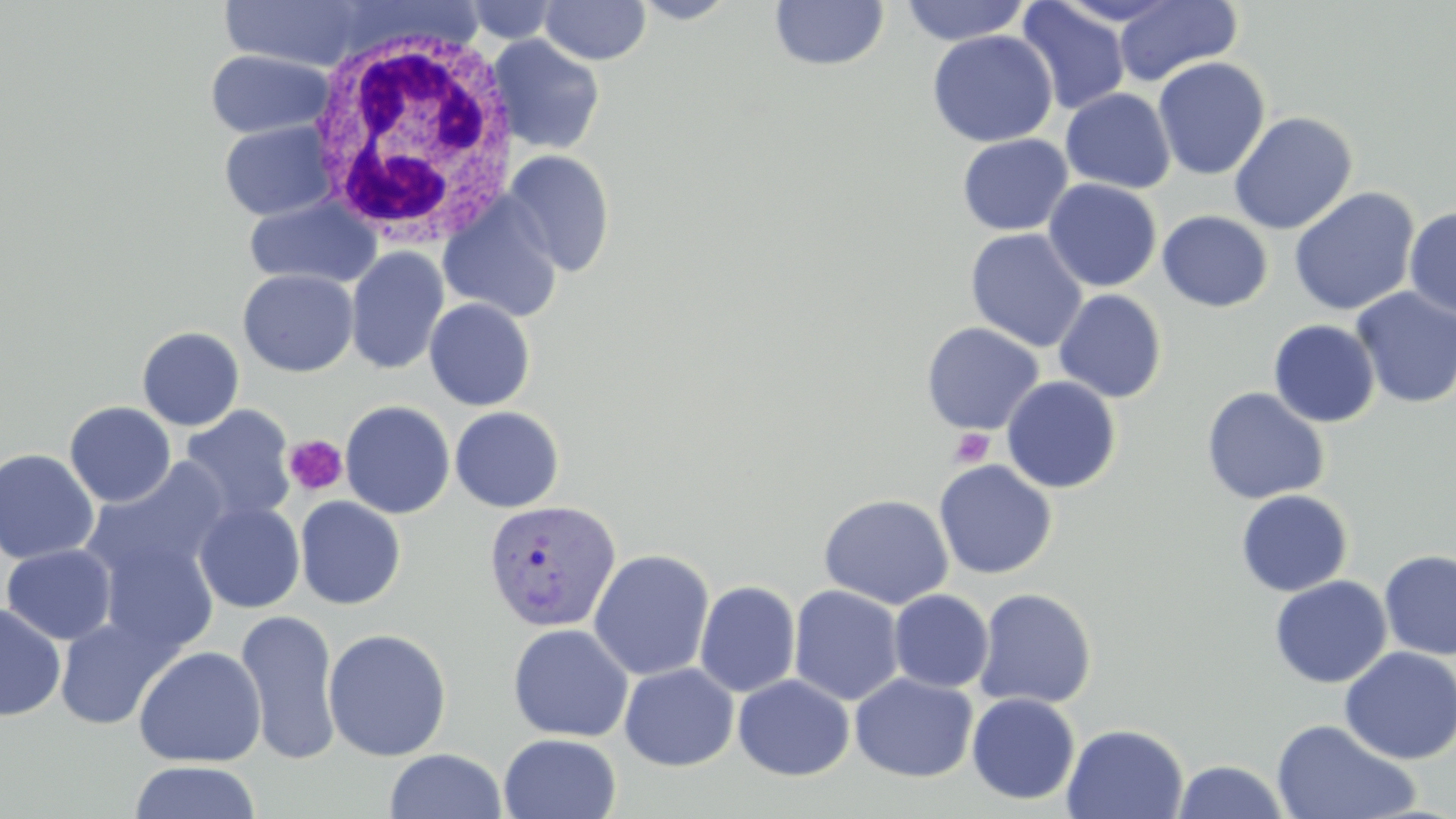

slide-level diagnosis = Plasmodium vivax
field of view = single
image size = 1456×819 pixels
white blood cell locations = approximate bounding boxes as [x1, y1, x2, y2] in pixels: [301, 24, 521, 251]
magnification = 1000x
preparation = thin blood smear
Plasmodium vivax-infected red blood cell locations = approximate bounding boxes as [x1, y1, x2, y2] in pixels: [482, 499, 622, 633]
uninfected red blood cell locations = approximate bounding boxes as [x1, y1, x2, y2] in pixels: [539, 0, 651, 65], [630, 0, 741, 24], [900, 0, 1031, 46], [1113, 0, 1242, 87], [219, 1, 374, 71], [461, 1, 564, 43], [768, 1, 890, 72], [1018, 1, 1131, 116], [927, 30, 1057, 148], [487, 34, 606, 155], [206, 48, 333, 139], [1153, 57, 1270, 180], [1060, 88, 1176, 193], [1229, 111, 1358, 234], [220, 119, 335, 221], [956, 134, 1073, 236], [502, 149, 615, 277], [1043, 178, 1163, 292], [1288, 187, 1421, 316], [438, 194, 564, 323], [244, 196, 378, 289], [1403, 207, 1456, 319], [1157, 210, 1273, 312], [965, 228, 1089, 352], [345, 246, 449, 375], [238, 269, 359, 377], [1350, 287, 1456, 409], [1053, 289, 1167, 403], [424, 298, 535, 411], [1268, 319, 1381, 428], [921, 322, 1044, 435], [136, 326, 244, 431], [1000, 376, 1121, 493], [1201, 387, 1329, 505], [340, 400, 455, 518], [64, 402, 176, 507], [179, 404, 297, 526], [450, 406, 565, 512], [0, 448, 99, 563], [80, 457, 233, 590], [934, 460, 1057, 579], [1235, 489, 1353, 596], [818, 493, 954, 609], [294, 496, 406, 610], [194, 501, 306, 613], [93, 534, 224, 657], [1, 543, 117, 645], [588, 549, 715, 681], [1378, 549, 1456, 661], [1269, 575, 1392, 688], [694, 580, 801, 697], [788, 585, 906, 707], [974, 587, 1097, 710], [888, 589, 993, 693], [0, 603, 66, 721], [236, 609, 342, 764], [54, 616, 178, 730], [507, 624, 633, 742], [322, 627, 452, 762], [132, 645, 267, 767], [1339, 646, 1456, 764], [619, 662, 739, 771], [849, 672, 978, 783], [733, 674, 855, 780], [967, 693, 1080, 805], [1271, 718, 1420, 819], [1061, 723, 1189, 819], [498, 733, 622, 819], [384, 748, 507, 819], [1172, 759, 1290, 818], [127, 760, 262, 819]
stain = May-Grünwald-Giemsa
platelet locations = approximate bounding boxes as [x1, y1, x2, y2] in pixels: [949, 427, 995, 468], [282, 434, 348, 497]
modality = optical microscopy